Point out each leukocyte.
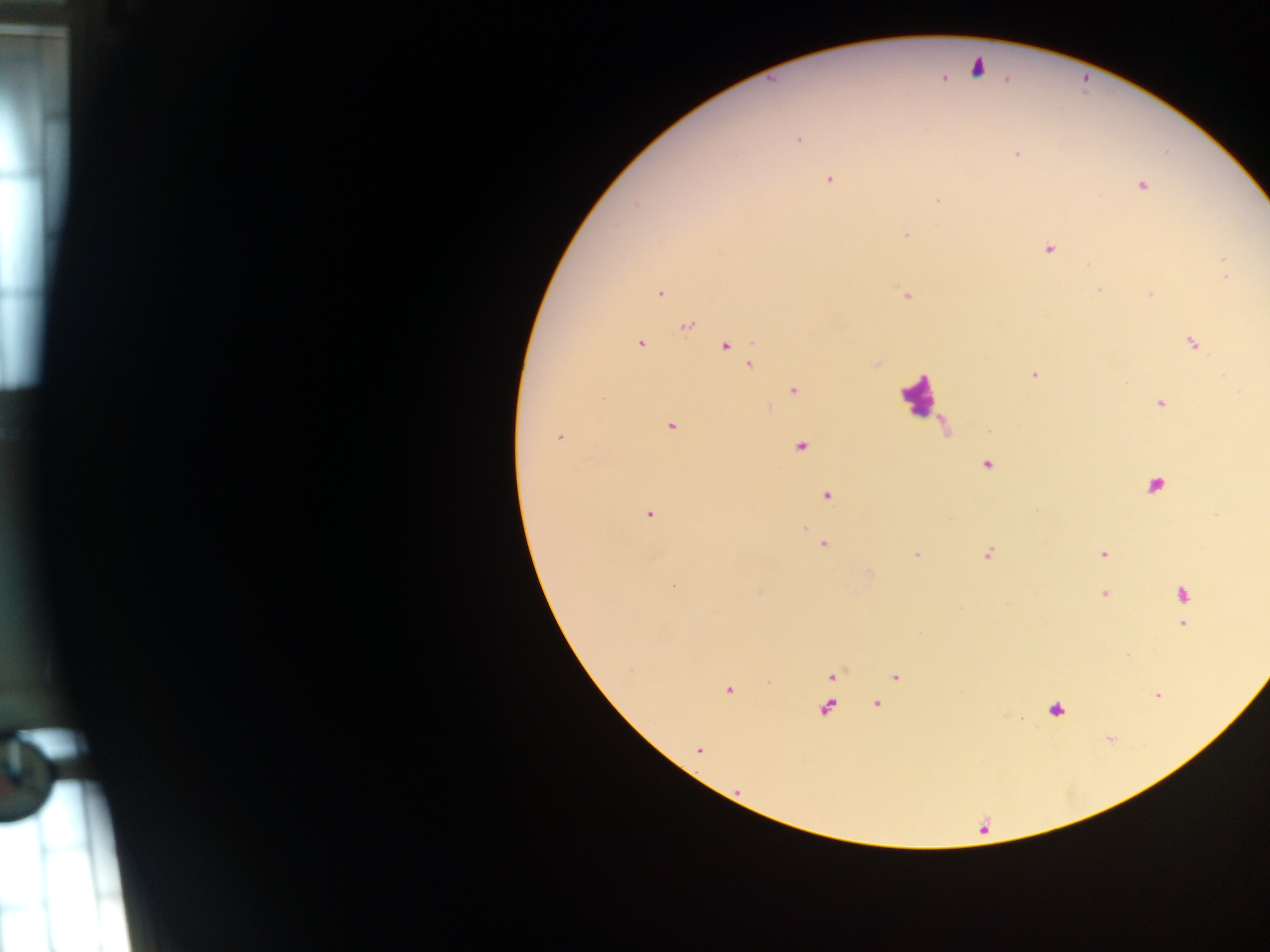
Approximate centers as {x, y} in pixels.
Leukocytes: {977, 67}, {918, 396}, {1156, 485}, {1056, 710}.

country: Ghana
malaria_parasite_locations: 'approximate centers as {x, y} in pixels: {942, 78}, {798, 138}, {1017, 153}, {829, 179}, {1140, 185}, {938, 200}, {906, 233}, {1049, 247}, {1223, 258}, {1088, 265}, {1226, 275}, {1099, 290}, {660, 293}, {1150, 294}, {906, 295}, {686, 326}, {640, 343}, {1192, 343}, {724, 345}, {749, 363}, {876, 363}, {1034, 374}, {792, 390}, {1160, 402}, {671, 426}, {989, 430}, {560, 437}, {800, 446}, {987, 464}, {826, 494}, {649, 513}, {1216, 515}, {804, 527}, {823, 544}, {988, 553}, {1102, 553}, {916, 554}, {759, 592}, {1105, 593}, {1182, 594}, {1183, 624}, {831, 676}, {895, 676}, {728, 689}, {1156, 694}, {875, 703}, {825, 708}, {699, 749}'
capture: mobile-phone photograph through a microscope
field_of_view: single
preparation: thick blood film
image_size: 1270×952 pixels